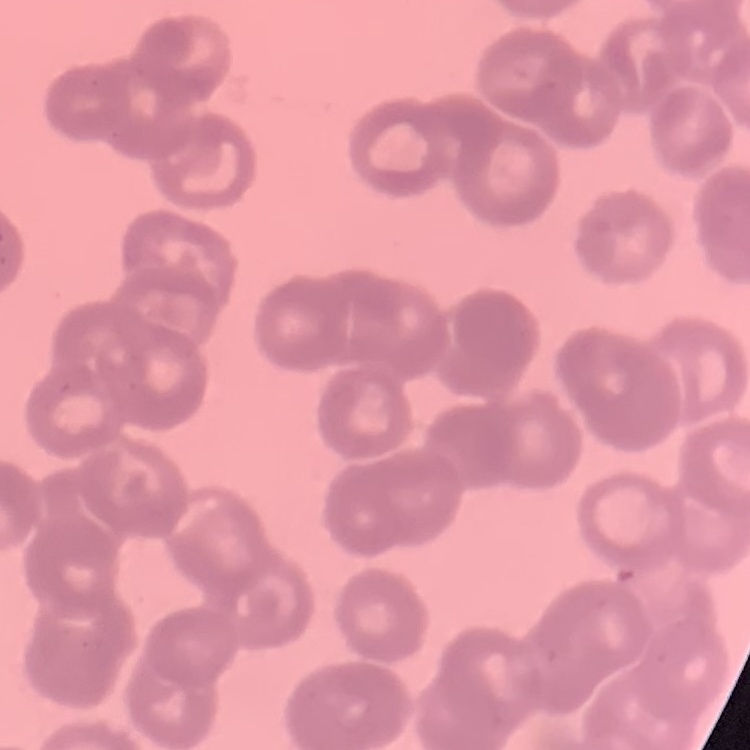
red_blood_cell_morphology: rouleaux formation
stain: Field's or Giemsa
preparation: thin peripheral smear
image_type: one tile cut from a larger photomicrograph